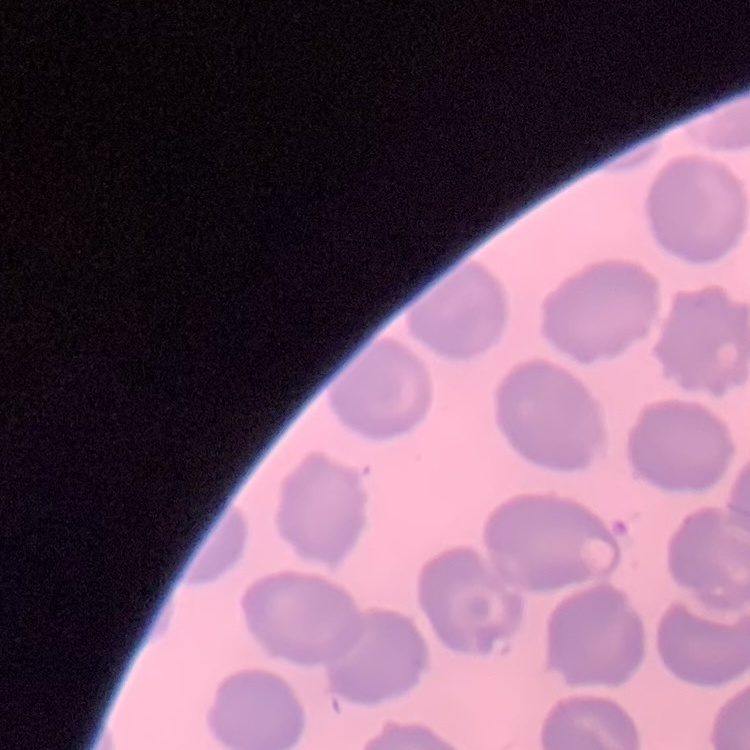
red blood cell morphology = no rouleaux formation
preparation = thin peripheral smear
stain = Field's or Giemsa
image type = square crop of a larger photomicrograph